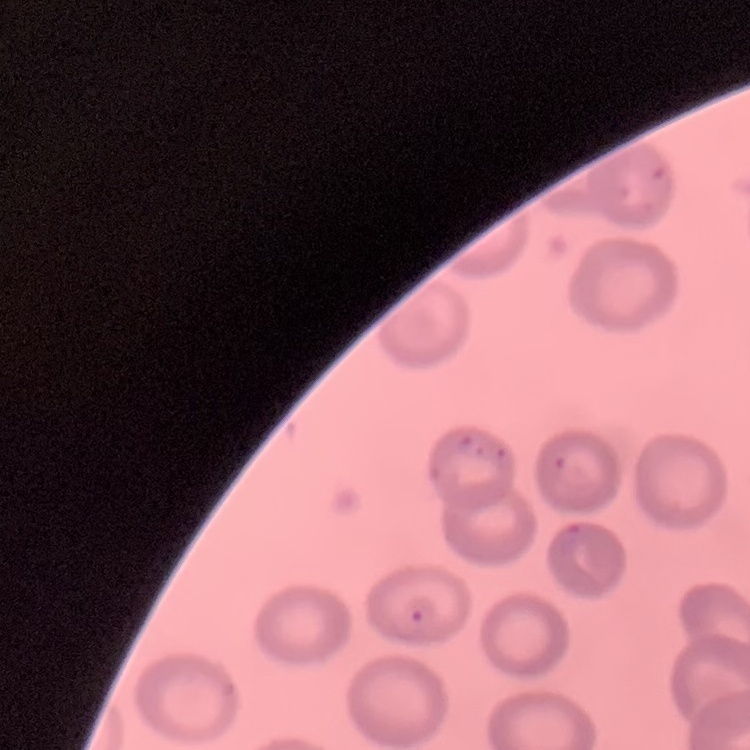
The erythrocytes show no rouleaux formation. Stained with either Field's or Giemsa. Thin blood smear. Square crop of a larger photomicrograph.